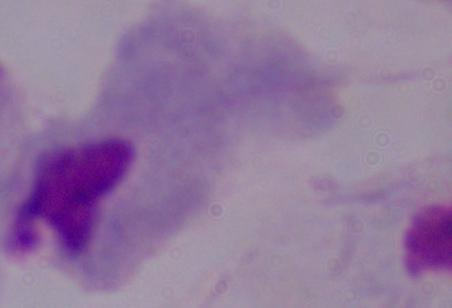

Summary:
  - Magnification: 1000x
  - Identification: trichomonad
  - Modality: micrograph